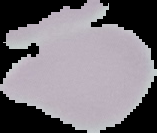
preparation: thin blood film
image_type: segmented cell region on a black background
image_size: 157×133 pixels
malaria_status: uninfected